Name the parasite shown.
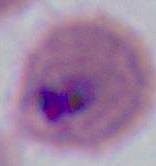
This is Plasmodium.

Photomicrograph. 400x or 1000x magnification.